Comment on the background quality.
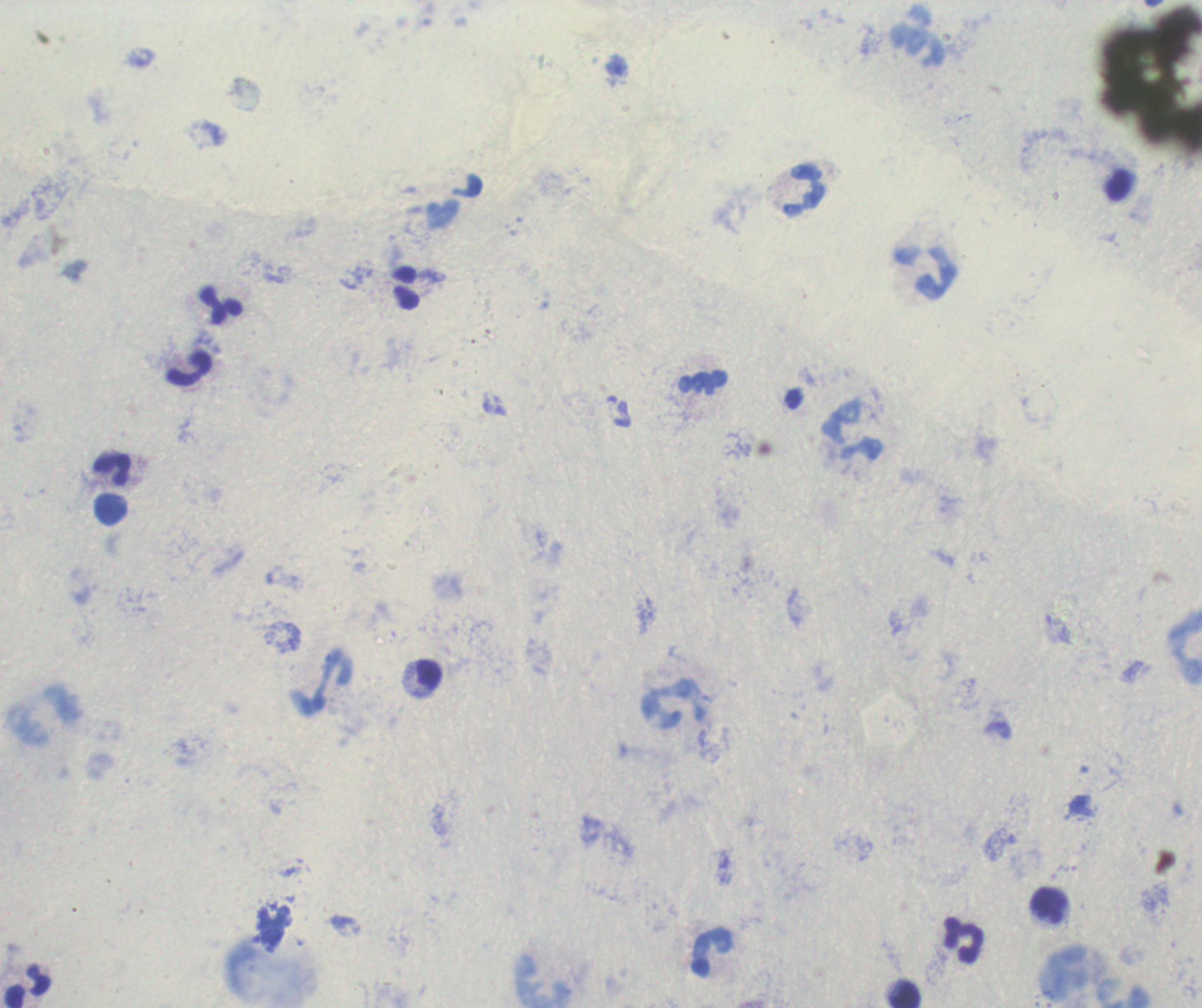
Poor.

Approximate centers as (x, y) in pixels. Leukocyte locations: (921, 38), (804, 191), (925, 272), (221, 305), (190, 368), (703, 384), (853, 431), (113, 470), (110, 510), (1185, 646), (428, 675), (324, 682), (674, 704), (1049, 905), (963, 939), (713, 953), (1065, 975), (29, 986), (905, 995). Previously used in a real diagnosis. Romanowsky-stained preparation. Single field of view. 100x magnification. Result: no Plasmodium parasites detected. Thick smear of blood. Image is 1202×1008 pixels.